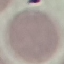 Result: no malaria parasites seen. Cell patch, automatically extracted from a larger field of view and resized to 64 × 64 pixels. Acquired by smartphone through the microscope eyepiece. Giemsa stain. Thin blood smear.